Report the malaria status of this cell.
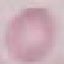

Uninfected.

Thin smear of blood. Automatically extracted cell patch, resized to 64 × 64 pixels. Acquired by smartphone through the microscope eyepiece. Giemsa stain.